Identify the blood parasite species.
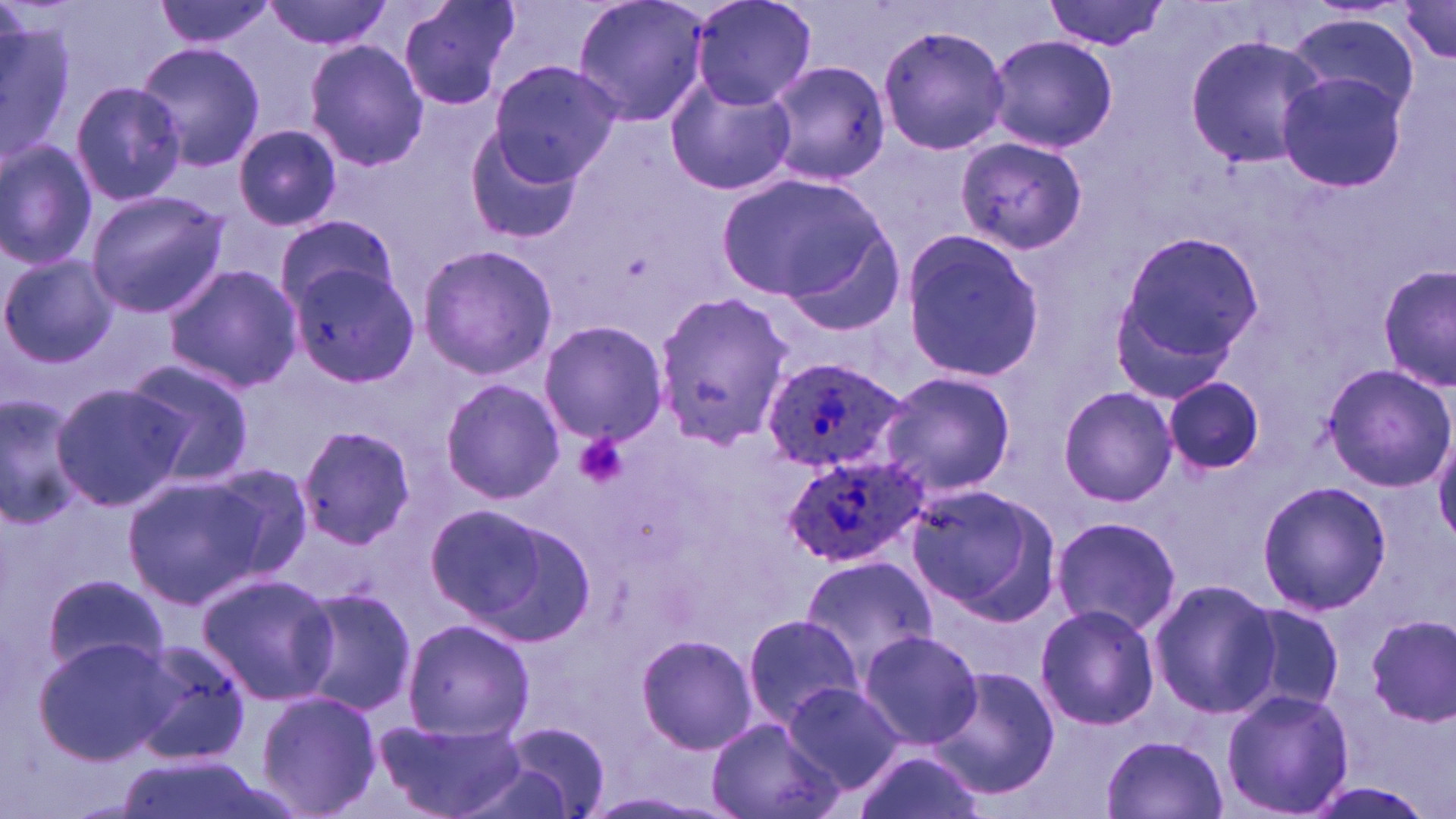

Plasmodium ovale.

Approximate bounding boxes as [x1, y1, x2, y2] in pixels. Platelet locations: [575, 432, 630, 489]. Plasmodium ovale-infected red blood cell locations: [761, 356, 909, 477], [782, 448, 928, 569]. Uninfected red blood cell locations: [152, 0, 276, 51], [264, 0, 396, 51], [399, 0, 522, 111], [572, 0, 711, 128], [691, 0, 817, 111], [1044, 0, 1169, 52], [1392, 0, 1456, 66], [0, 10, 73, 167], [1285, 11, 1424, 120], [877, 23, 1010, 157], [986, 34, 1118, 154], [1183, 34, 1328, 170], [304, 40, 430, 171], [134, 41, 264, 175], [764, 56, 889, 187], [486, 59, 621, 186], [1276, 68, 1409, 194], [665, 76, 797, 197], [69, 82, 187, 207], [463, 119, 585, 247], [234, 124, 341, 232], [955, 136, 1090, 257], [0, 138, 99, 272], [715, 171, 886, 305], [85, 190, 230, 317], [273, 218, 399, 313], [899, 227, 1044, 379], [787, 228, 907, 337], [1111, 231, 1261, 393], [416, 243, 557, 380], [2, 255, 118, 366], [1378, 264, 1456, 391], [163, 265, 303, 392], [288, 265, 418, 389], [648, 292, 796, 448], [538, 321, 668, 446], [120, 358, 258, 487], [1320, 363, 1455, 491], [877, 370, 1017, 498], [1163, 374, 1266, 476], [439, 378, 564, 504], [51, 381, 190, 512], [1058, 387, 1177, 507], [0, 394, 88, 528], [293, 424, 417, 551], [1432, 425, 1456, 544], [200, 460, 317, 580], [122, 475, 268, 610], [1254, 478, 1392, 616], [904, 483, 1060, 623], [429, 504, 595, 647], [1050, 514, 1180, 636], [797, 554, 939, 682], [40, 570, 172, 681], [194, 571, 339, 706], [1148, 579, 1280, 719], [289, 585, 416, 718], [1235, 602, 1345, 715], [1035, 603, 1161, 731], [739, 613, 867, 729], [1361, 614, 1454, 726], [400, 617, 534, 741], [858, 630, 984, 750], [635, 634, 759, 755], [32, 637, 173, 765], [124, 638, 253, 767], [931, 668, 1062, 798], [782, 681, 906, 791], [1220, 688, 1355, 818], [255, 690, 382, 818], [374, 718, 527, 819], [705, 718, 846, 819], [496, 721, 613, 817], [1102, 735, 1227, 819], [853, 748, 983, 819], [117, 750, 266, 819], [1302, 781, 1436, 817]. 1000x magnification. Optical microscopy. May-Grünwald-Giemsa-stained preparation. Image is 1456×819 pixels. Single field of view. Thin blood smear.